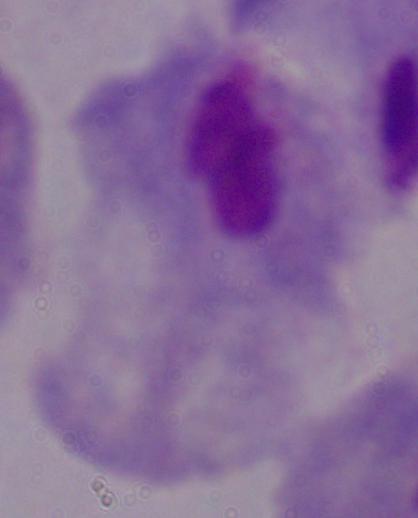
Summary:
  - Magnification: 1000x
  - Modality: photomicrograph
  - Identification: trichomonad